Outline platelets.
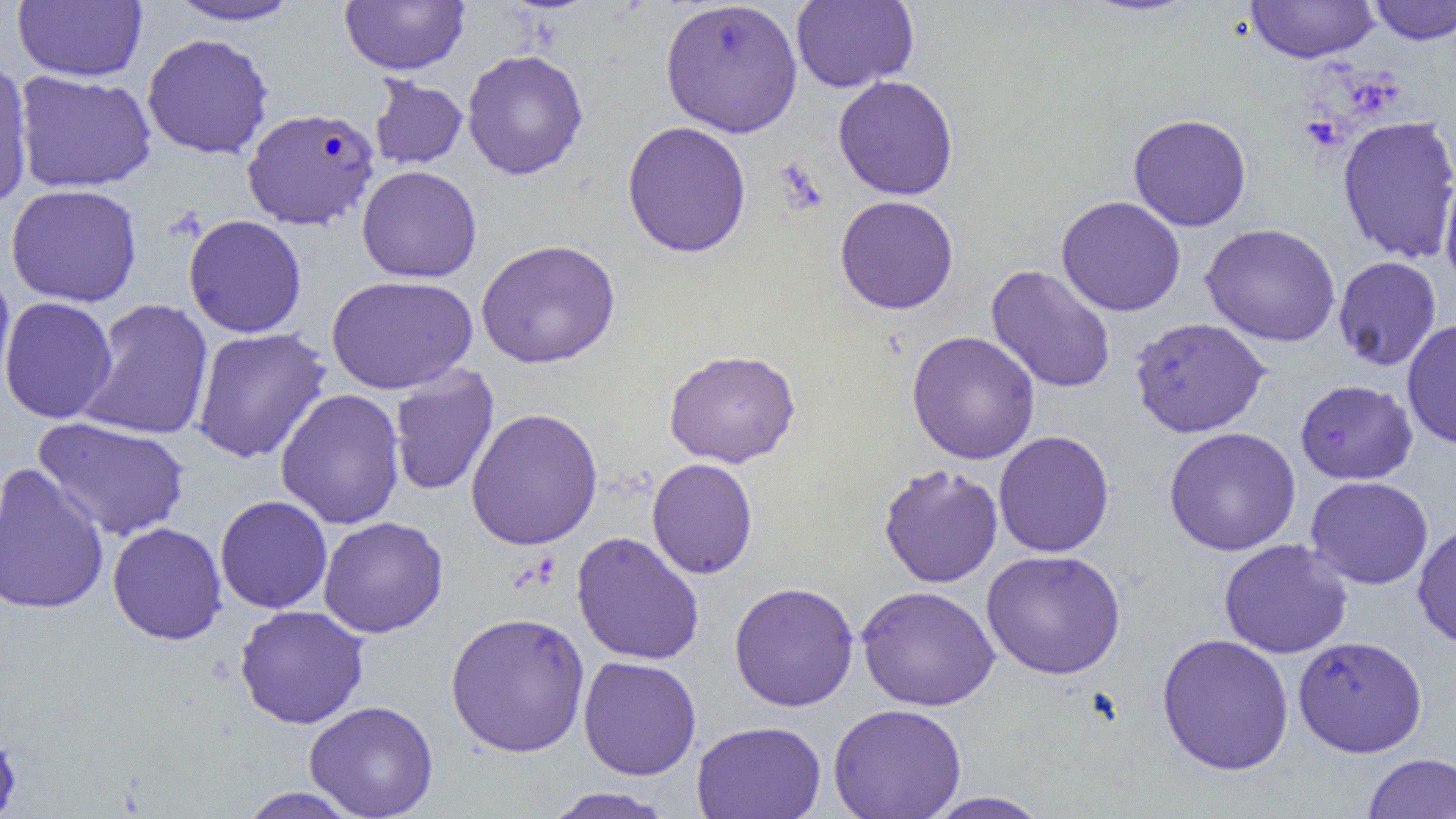
Approximate bounding boxes as [x1, y1, x2, y2] in pixels.
Platelets: [1301, 113, 1347, 154].

slide-level diagnosis = Plasmodium falciparum
image size = 1456×819 pixels
Plasmodium falciparum-infected red blood cell locations = approximate bounding boxes as [x1, y1, x2, y2] in pixels: [242, 107, 379, 229]
preparation = thin blood smear
magnification = 1000x
uninfected red blood cell locations = approximate bounding boxes as [x1, y1, x2, y2] in pixels: [12, 0, 147, 82], [791, 0, 919, 93], [165, 1, 305, 26], [340, 1, 469, 75], [660, 1, 803, 137], [1245, 1, 1380, 63], [1368, 1, 1456, 44], [142, 33, 274, 159], [462, 49, 588, 180], [0, 60, 34, 208], [13, 71, 157, 193], [369, 75, 468, 169], [833, 75, 959, 200], [1127, 113, 1252, 231], [1337, 115, 1456, 264], [622, 121, 752, 258], [356, 165, 482, 283], [1439, 168, 1456, 295], [5, 184, 143, 307], [834, 195, 959, 314], [1056, 195, 1186, 317], [183, 214, 307, 338], [1201, 223, 1341, 347], [476, 239, 621, 369], [1332, 256, 1442, 371], [986, 264, 1116, 394], [0, 270, 16, 405], [326, 275, 478, 394], [0, 296, 117, 423], [77, 298, 214, 441], [1129, 317, 1271, 438], [1401, 319, 1456, 450], [192, 327, 331, 463], [906, 330, 1040, 465], [663, 348, 801, 468], [388, 366, 500, 497], [1294, 379, 1418, 484], [275, 388, 406, 529], [465, 407, 603, 550], [33, 416, 190, 540], [1163, 427, 1301, 556], [994, 430, 1115, 557], [646, 458, 758, 579], [0, 464, 110, 615], [878, 464, 1004, 588], [1305, 475, 1434, 589], [215, 495, 332, 614], [318, 515, 448, 638], [107, 522, 227, 645], [1412, 522, 1456, 648], [571, 531, 705, 665], [1218, 539, 1353, 659], [981, 549, 1126, 679], [729, 581, 859, 711], [856, 585, 1000, 711], [234, 604, 369, 729], [445, 611, 590, 757], [1156, 633, 1294, 775], [1293, 635, 1428, 757], [578, 655, 701, 780], [304, 700, 439, 818], [828, 703, 967, 819], [692, 720, 827, 819], [0, 728, 21, 819], [1362, 753, 1456, 819], [541, 786, 677, 819], [238, 787, 364, 819], [922, 791, 1053, 818]
modality = light microscopy
field of view = single